State which parasite is depicted.
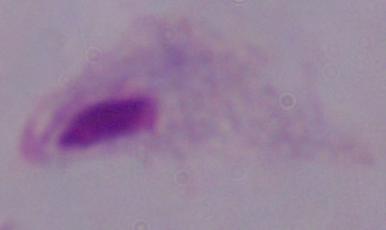
A trichomonad.

Summary:
  - Magnification: 1000x
  - Modality: photomicrograph